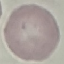
{
  "result": "no malaria parasites seen",
  "stain": "Giemsa",
  "image_type": "automatically extracted cell patch, resized to 64 × 64 pixels",
  "preparation": "thin smear",
  "capture": "smartphone camera at the microscope eyepiece"
}